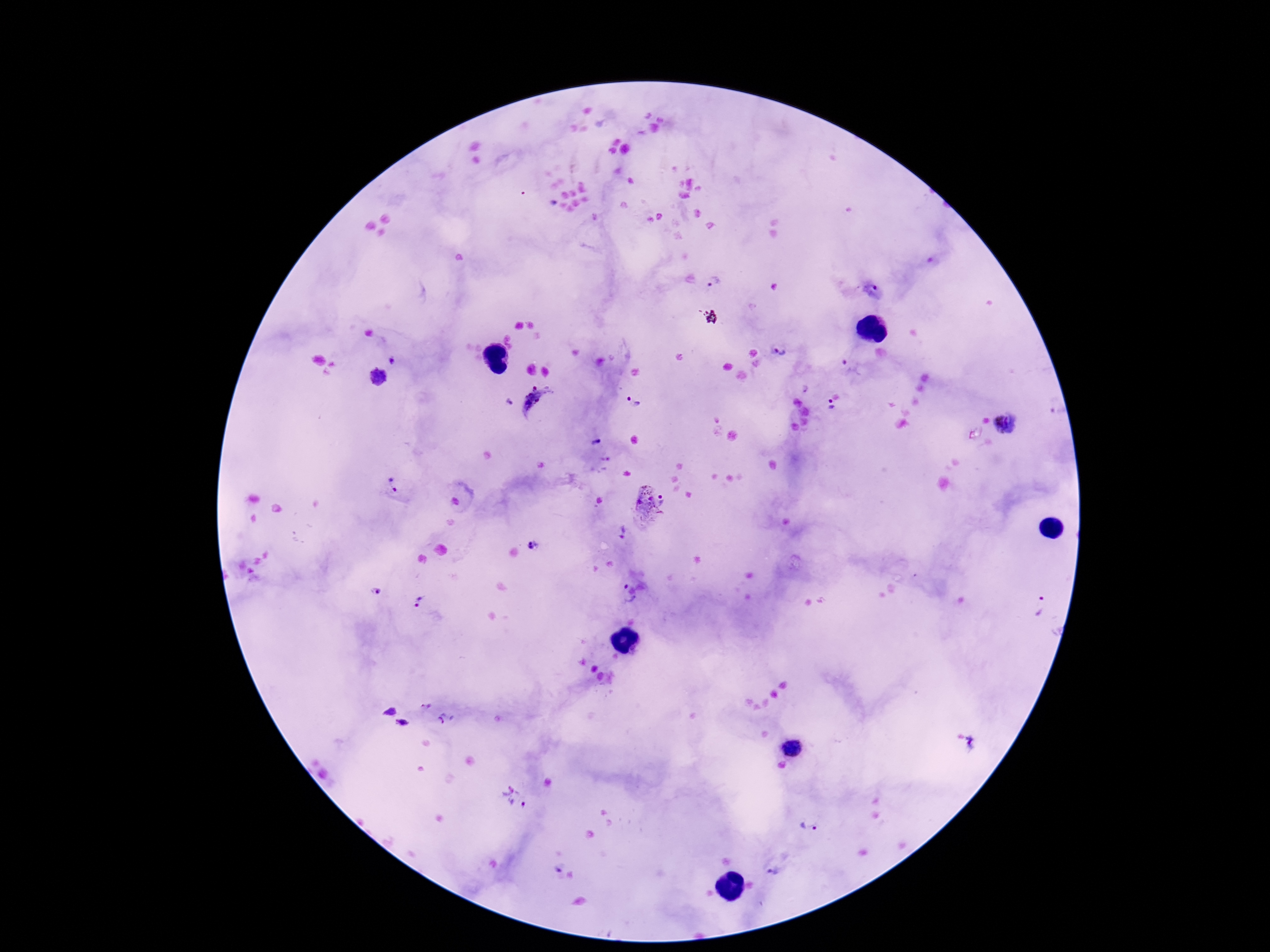 Approximate centers as [x, y] in pixels. Plasmodium parasite locations: [716, 282], [874, 292], [781, 351], [392, 361], [378, 378], [804, 390], [540, 401], [508, 402], [634, 403], [830, 408], [1005, 424], [596, 443], [392, 485], [649, 503], [623, 532], [534, 545], [625, 586], [375, 591], [420, 602], [633, 603], [1041, 608], [426, 706], [389, 711], [447, 718], [402, 723], [977, 743], [793, 747], [514, 798], [807, 826], [775, 871]. Thick blood film. Photographed through the microscope eyepiece with a smartphone camera. Giemsa-stained preparation. One field from this slide. Image is 1270×952 pixels. 100x magnification. Patient malaria status: positive.